State which cell type is depicted.
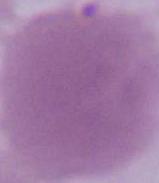

This is an erythrocyte.

magnification = 1000x
modality = photomicrograph